Assess this cell for malaria.
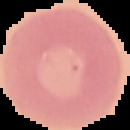

Uninfected.

Segmented cell region on a black background. Image is 130×130 pixels. From a thin blood film.